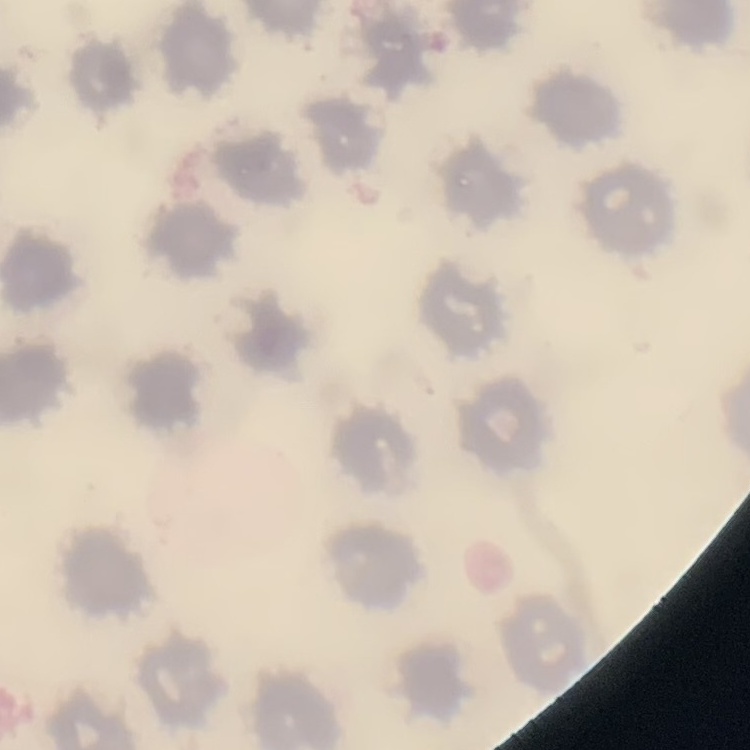

Summary:
  - Erythrocyte morphology: no rouleaux formation
  - Preparation: thin peripheral smear
  - Image type: square crop of a larger photomicrograph
  - Stain: Field's or Giemsa